Locate every malaria parasite and every leukocyte.
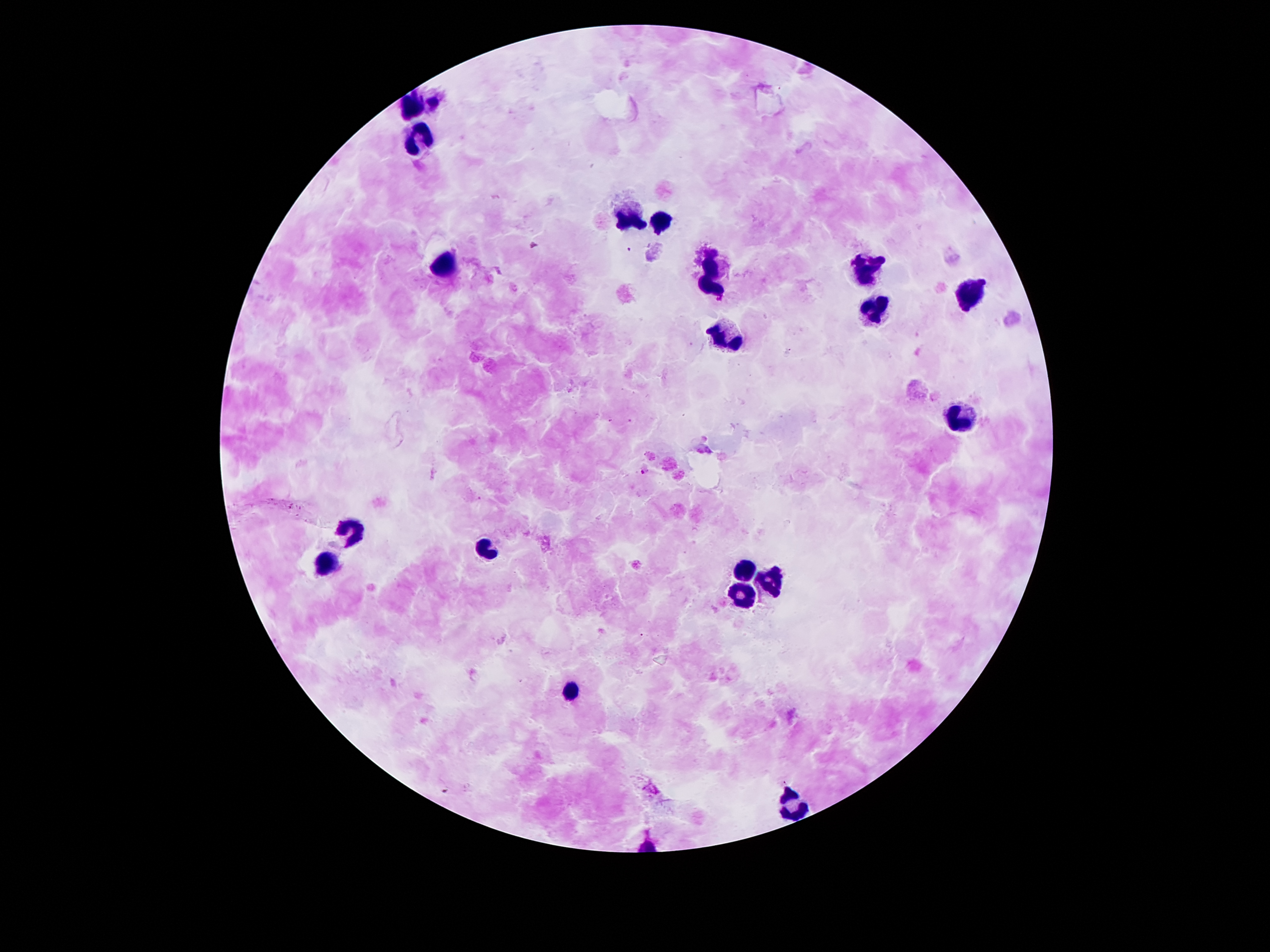
Approximate centers as (x, y) in pixels.
Malaria parasites: (630, 249), (644, 469).
Leukocytes: (436, 103), (412, 105), (417, 139), (629, 218), (659, 226), (446, 262), (864, 268), (708, 273), (968, 295), (872, 306), (721, 332), (958, 417), (353, 532), (481, 546), (323, 563), (741, 571), (770, 581), (741, 596), (570, 692), (790, 799).

{
  "patient_malaria_status": "positive for Plasmodium falciparum",
  "stain": "Giemsa",
  "image_size": "1270×952 pixels",
  "field_of_view": "single",
  "capture": "smartphone camera through the microscope eyepiece",
  "magnification": "100x",
  "preparation": "thick peripheral-blood smear"
}